Identify the preparation type.
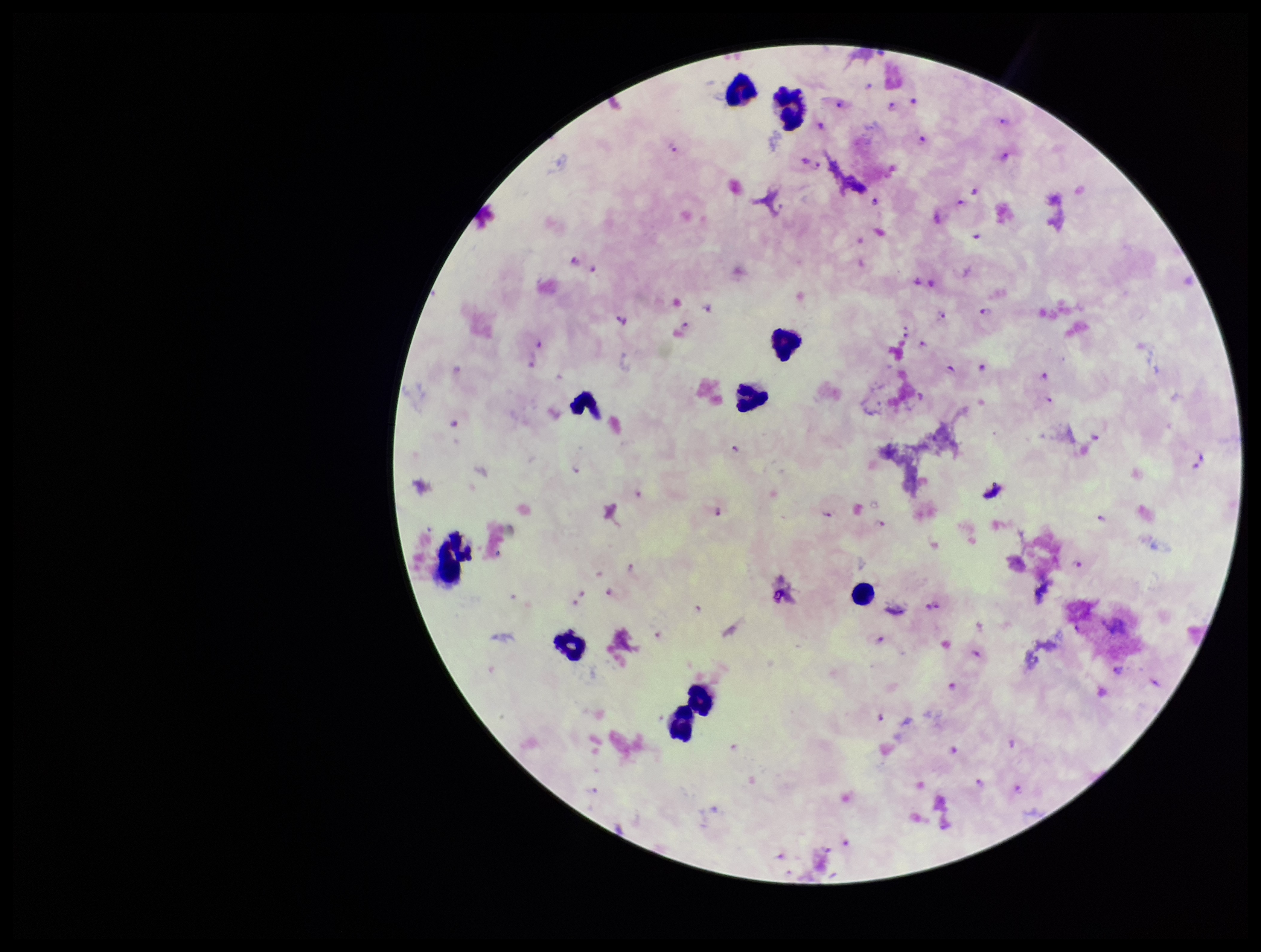

Thick.

Patient malaria status: infected. Photographed through the microscope eyepiece with a smartphone camera. Stained with Giemsa. Plasmodium parasites: detected. Leukocyte count: 10. Parasite count: 93. Single field of view. Image is 1261×952 pixels. Species reported for this patient: Plasmodium falciparum.